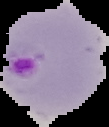
Summary:
  - Image type: segmented cell region with the area outside set to black
  - Image size: 109×127 pixels
  - Preparation: thin blood film
  - Result: Plasmodium parasites identified